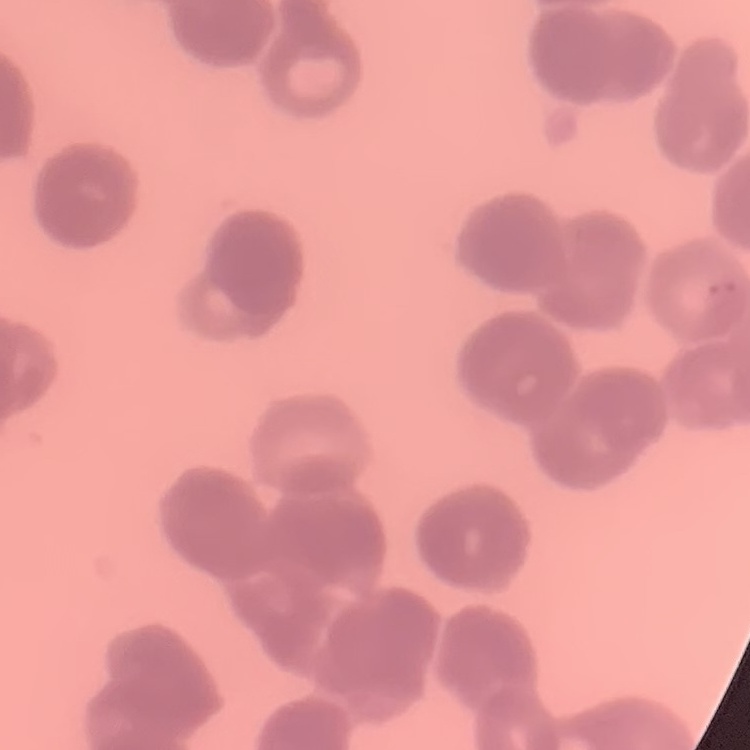

The red blood cells exhibit rouleaux formation. One tile cut from a larger photomicrograph. Thin blood film. Stained with either Field's or Giemsa.